Point out each malaria parasite.
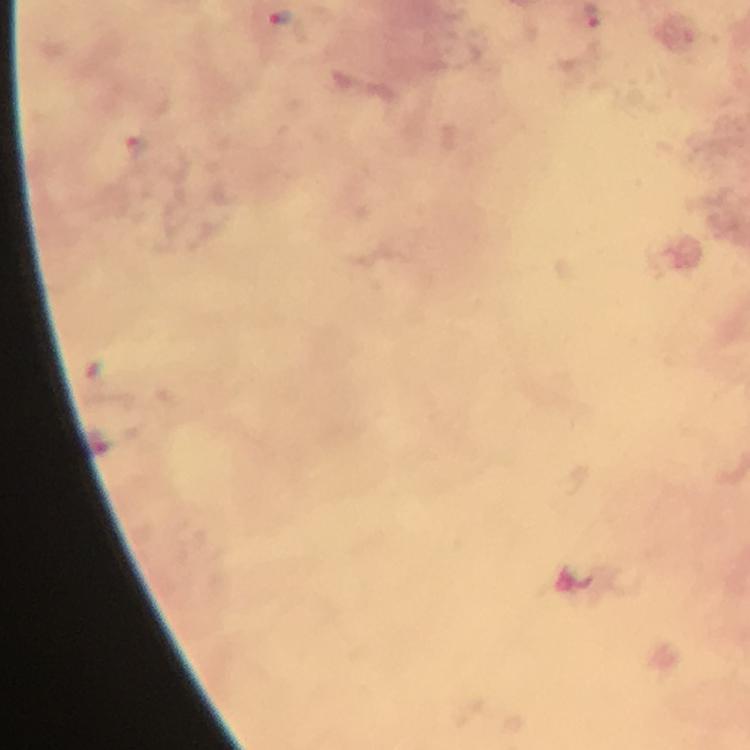

Approximate centers as [x, y] in pixels.
Malaria parasites: [279, 17].

Summary:
  - Preparation: thick smear
  - Image size: 750×750 pixels
  - Magnification: 100x
  - Immersion oil: applied
  - Capture: smartphone photograph through a microscope
  - Context: from a diagnostic examination for malaria
  - Stain: Giemsa
  - Cropped from: a single field of view